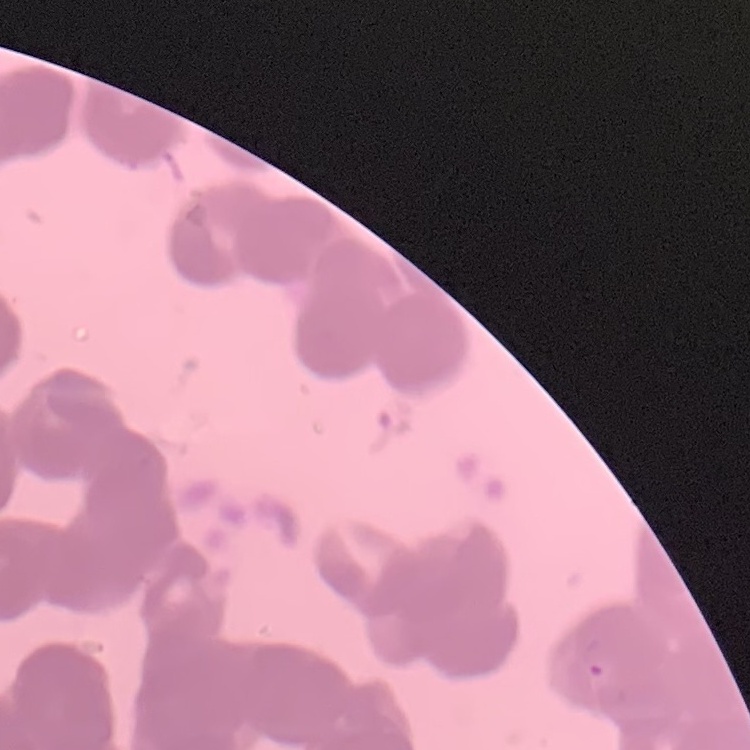
{
  "erythrocyte_morphology": "rouleaux formation",
  "stain": "Field's or Giemsa",
  "image_type": "one tile cut from a larger photomicrograph",
  "preparation": "thin blood smear"
}